Describe the morphology of the red blood cells.
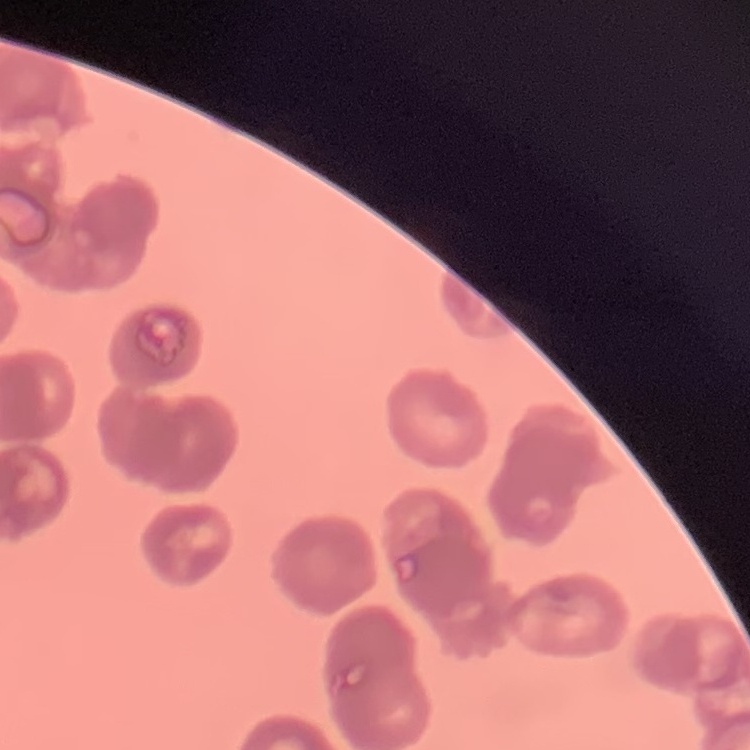
Rouleaux formation.

preparation = thin peripheral smear
image type = square crop of a larger photomicrograph
stain = Field's or Giemsa